Comment on the morphology of the erythrocytes.
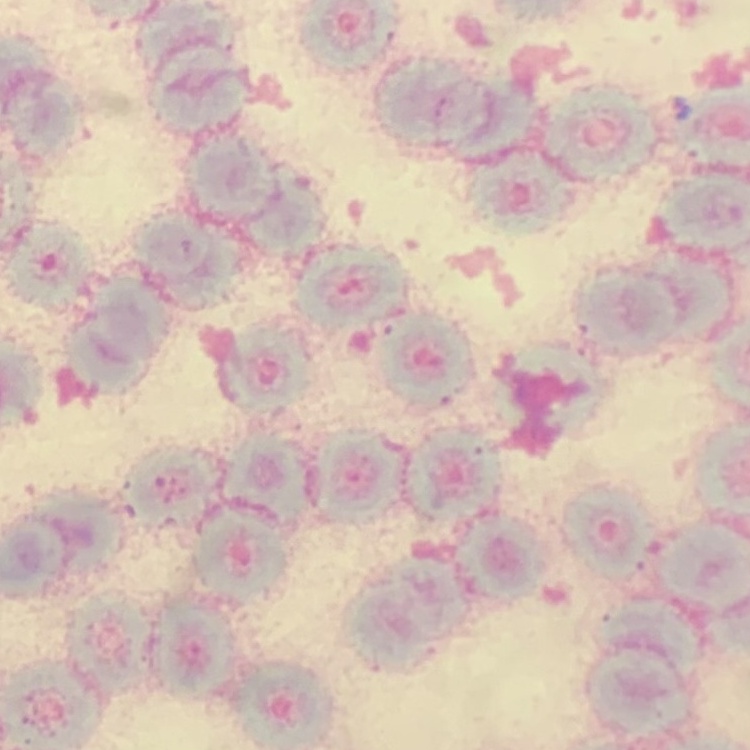
They show rouleaux formation.

Thin blood film. Stained with either Field's or Giemsa. Square crop of a larger photomicrograph.